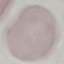
Malaria status: uninfected. Automatically extracted cell patch, resized to 64 × 64 pixels. Thin blood smear. Acquired by smartphone through the microscope eyepiece. Giemsa stain.